Assess this cell for malaria.
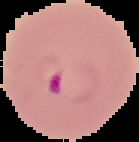
Parasitized.

Summary:
  - Image type: segmented cell region with the area outside set to black
  - Image size: 139×142 pixels
  - Preparation: thin blood smear